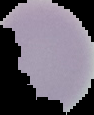

{
  "result": "no malaria parasites detected",
  "preparation": "thin blood film",
  "image_type": "segmented cell region on a black background",
  "image_size": "94×115 pixels"
}